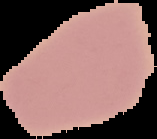
{
  "preparation": "thin blood smear",
  "result": "no Plasmodium parasites detected",
  "image_type": "segmented cell region on a black background",
  "image_size": "157×139 pixels"
}